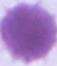
1000x magnification. A red blood cell is seen. Photomicrograph.